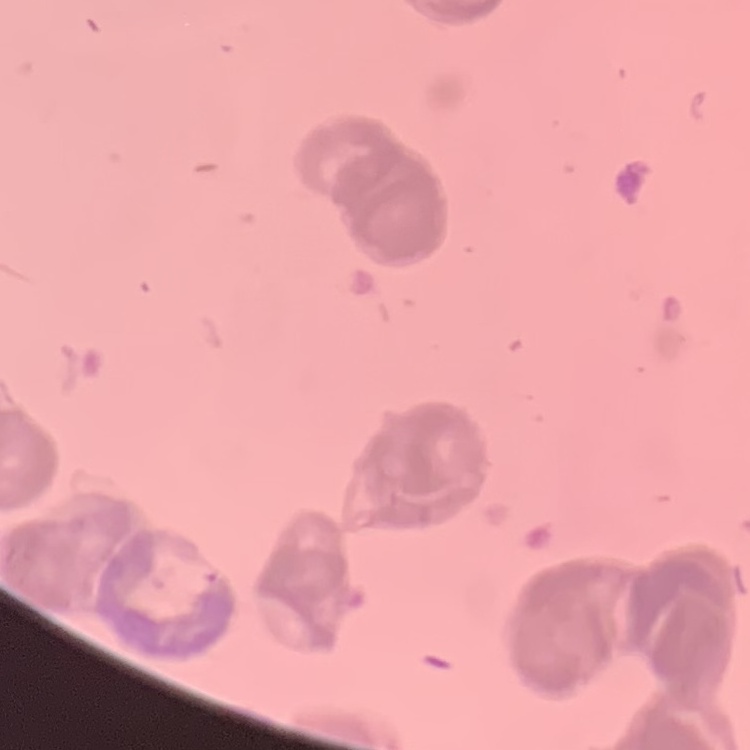

The erythrocytes exhibit rouleaux formation. Stained with either Field's or Giemsa. Thin blood film. Square crop of a larger photomicrograph.